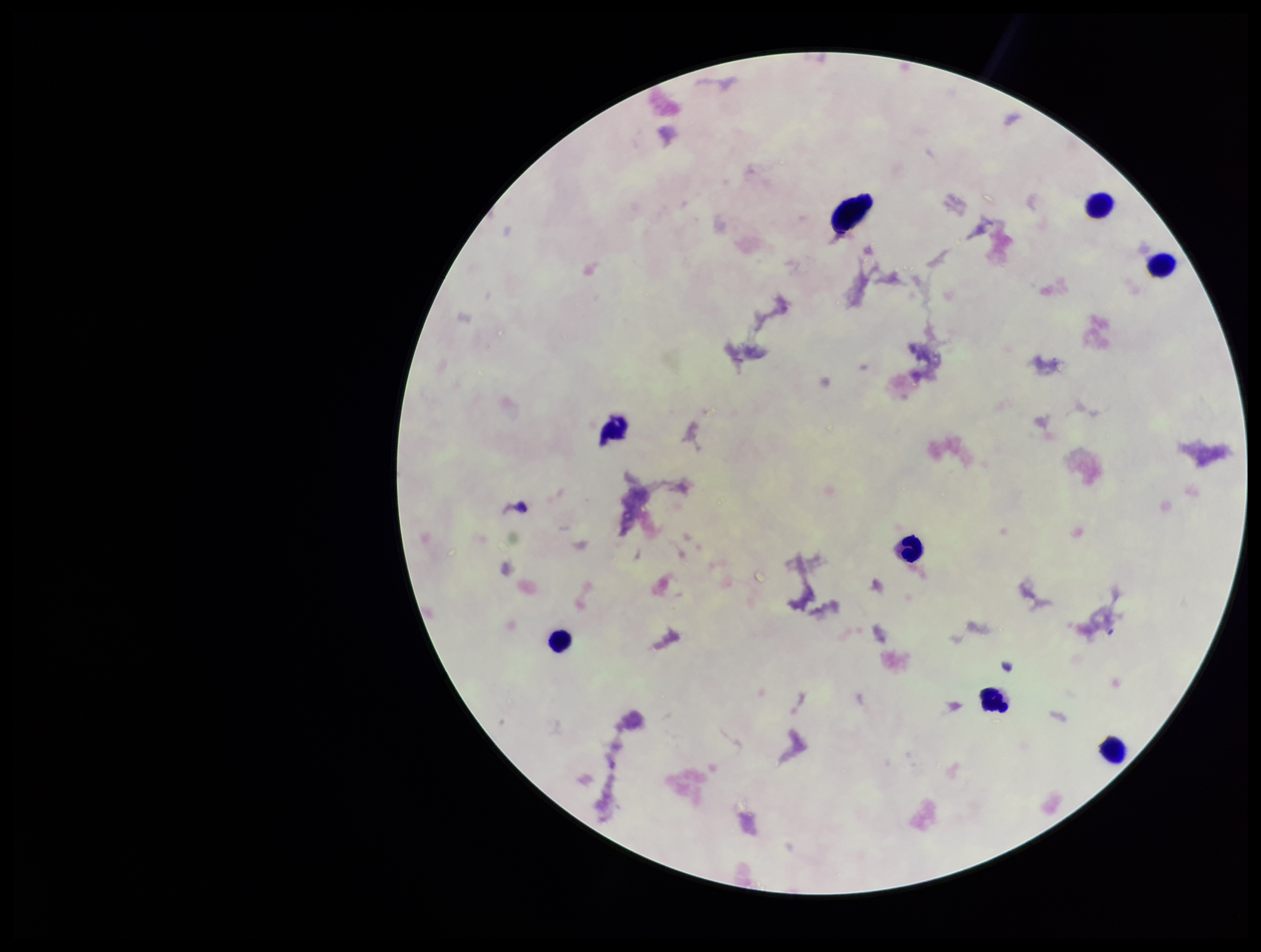
stain: Giemsa
parasite_count: 0
image_size: 1261×952 pixels
preparation: thick blood smear
field_of_view: single
leukocyte_count: 7
capture: smartphone photograph through the microscope eyepiece
plasmodium_parasites: none detected
patient_malaria_status: negative